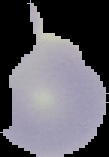 From a thin blood film. Malaria status: uninfected. Cell region segmented out of the field of view; the surrounding area is masked to black. Image is 109×157 pixels.